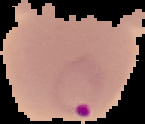
{
  "image_size": "145×124 pixels",
  "image_type": "segmented cell region with the area outside set to black",
  "malaria_status": "parasitized",
  "preparation": "thin blood smear"
}